Report the malaria status of this cell.
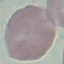
Uninfected.

preparation = thin blood film
stain = Giemsa
capture = smartphone through the microscope eyepiece
image type = cell patch, automatically extracted from a larger field of view and resized to 64 × 64 pixels